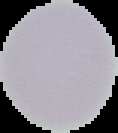 Image is 118×133 pixels. From a thin blood smear. Result: no Plasmodium parasites seen. Cell region segmented out of the field of view; the surrounding area is masked to black.